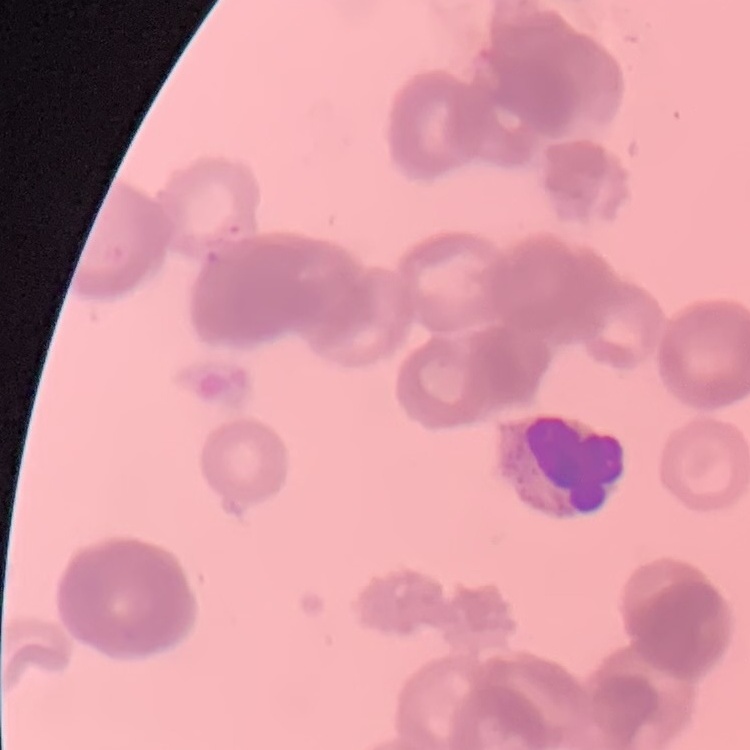

Summary:
  - Red blood cell morphology: rouleaux formation
  - Stain: Field's or Giemsa
  - Image type: one tile cut from a larger photomicrograph
  - Preparation: thin blood film